Assess this cell for malaria.
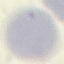
It is uninfected.

Summary:
  - Preparation: thin blood smear
  - Capture: smartphone through the microscope eyepiece
  - Stain: Giemsa
  - Image type: cell patch, automatically extracted from a larger field of view and resized to 64 × 64 pixels